Classify this cell by malaria status.
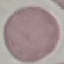
It is uninfected.

Acquired by smartphone through the microscope eyepiece. Automatically extracted cell patch, resized to 64 × 64 pixels. Giemsa stain. Thin blood smear.